Report the malaria status of this cell.
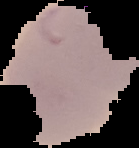
It is parasitized.

Segmented cell region on a black background. Image is 139×148 pixels. From a thin blood smear.